Locate every Plasmodium falciparum-infected red blood cell.
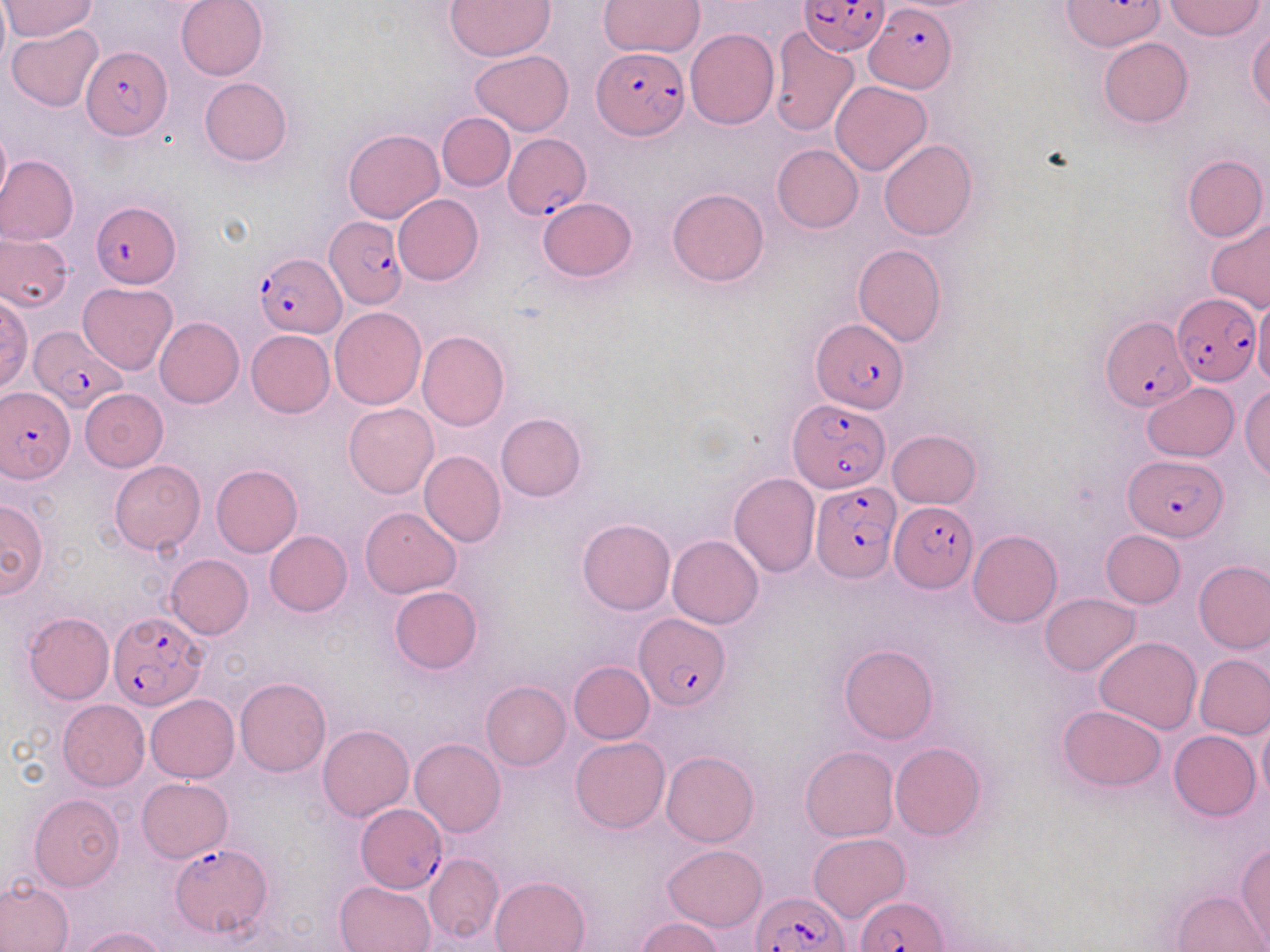
Approximate bounding boxes as named x1/y1/x2/y2 corners in pixels.
Plasmodium falciparum-infected red blood cells: (x1=800, y1=1, x2=890, y2=56), (x1=864, y1=6, x2=955, y2=92), (x1=79, y1=45, x2=172, y2=140), (x1=593, y1=46, x2=689, y2=139), (x1=504, y1=133, x2=593, y2=219), (x1=91, y1=200, x2=181, y2=287), (x1=325, y1=217, x2=407, y2=308), (x1=257, y1=254, x2=344, y2=337), (x1=1172, y1=294, x2=1260, y2=385), (x1=1099, y1=314, x2=1194, y2=412), (x1=809, y1=319, x2=909, y2=412), (x1=29, y1=323, x2=125, y2=412), (x1=2, y1=388, x2=74, y2=480), (x1=787, y1=397, x2=891, y2=492), (x1=1124, y1=454, x2=1228, y2=539), (x1=810, y1=480, x2=900, y2=582), (x1=888, y1=501, x2=974, y2=592), (x1=107, y1=610, x2=208, y2=711), (x1=634, y1=612, x2=731, y2=711), (x1=355, y1=804, x2=448, y2=892), (x1=169, y1=843, x2=274, y2=939), (x1=751, y1=891, x2=852, y2=952), (x1=853, y1=896, x2=947, y2=951).

Uninfected red blood cell locations: (x1=0, y1=0, x2=10, y2=69), (x1=175, y1=0, x2=269, y2=81), (x1=445, y1=0, x2=555, y2=59), (x1=1165, y1=0, x2=1264, y2=41), (x1=1, y1=1, x2=99, y2=42), (x1=598, y1=1, x2=705, y2=56), (x1=7, y1=24, x2=104, y2=112), (x1=769, y1=27, x2=860, y2=137), (x1=1247, y1=27, x2=1270, y2=113), (x1=685, y1=28, x2=780, y2=129), (x1=1098, y1=38, x2=1192, y2=128), (x1=469, y1=51, x2=573, y2=135), (x1=199, y1=77, x2=292, y2=166), (x1=832, y1=81, x2=932, y2=175), (x1=437, y1=112, x2=515, y2=192), (x1=0, y1=123, x2=12, y2=209), (x1=343, y1=128, x2=443, y2=222), (x1=878, y1=138, x2=978, y2=240), (x1=772, y1=144, x2=862, y2=233), (x1=0, y1=155, x2=78, y2=245), (x1=1181, y1=155, x2=1267, y2=242), (x1=667, y1=188, x2=768, y2=287), (x1=393, y1=194, x2=483, y2=285), (x1=536, y1=198, x2=636, y2=281), (x1=1206, y1=218, x2=1270, y2=313), (x1=1, y1=232, x2=72, y2=311), (x1=853, y1=244, x2=947, y2=346), (x1=79, y1=282, x2=177, y2=375), (x1=0, y1=293, x2=33, y2=393), (x1=1254, y1=296, x2=1270, y2=393), (x1=330, y1=307, x2=425, y2=409), (x1=154, y1=317, x2=244, y2=408), (x1=246, y1=330, x2=334, y2=417), (x1=417, y1=330, x2=510, y2=432), (x1=1141, y1=382, x2=1239, y2=462), (x1=1240, y1=386, x2=1269, y2=480), (x1=80, y1=389, x2=168, y2=470), (x1=344, y1=402, x2=438, y2=498), (x1=496, y1=412, x2=587, y2=501), (x1=887, y1=430, x2=981, y2=508), (x1=420, y1=450, x2=506, y2=548), (x1=109, y1=461, x2=204, y2=554), (x1=211, y1=464, x2=302, y2=557), (x1=729, y1=473, x2=819, y2=577), (x1=0, y1=499, x2=49, y2=597), (x1=359, y1=507, x2=462, y2=597), (x1=577, y1=518, x2=674, y2=615), (x1=1101, y1=530, x2=1186, y2=608), (x1=265, y1=531, x2=352, y2=616), (x1=968, y1=531, x2=1061, y2=627), (x1=668, y1=535, x2=763, y2=629), (x1=166, y1=555, x2=253, y2=639), (x1=1194, y1=561, x2=1270, y2=654), (x1=389, y1=586, x2=482, y2=674), (x1=1040, y1=593, x2=1139, y2=675), (x1=23, y1=612, x2=114, y2=704), (x1=1095, y1=636, x2=1202, y2=734), (x1=839, y1=645, x2=937, y2=744), (x1=1186, y1=654, x2=1265, y2=819), (x1=1194, y1=654, x2=1270, y2=738), (x1=569, y1=661, x2=654, y2=744), (x1=234, y1=678, x2=330, y2=776), (x1=481, y1=681, x2=571, y2=770), (x1=147, y1=694, x2=238, y2=782), (x1=57, y1=699, x2=149, y2=791), (x1=1057, y1=705, x2=1165, y2=791), (x1=1257, y1=714, x2=1270, y2=806), (x1=318, y1=725, x2=414, y2=821), (x1=1169, y1=729, x2=1260, y2=820), (x1=571, y1=737, x2=669, y2=833), (x1=409, y1=739, x2=505, y2=837), (x1=890, y1=742, x2=986, y2=840), (x1=800, y1=746, x2=898, y2=841), (x1=662, y1=750, x2=758, y2=846), (x1=137, y1=778, x2=233, y2=862), (x1=30, y1=793, x2=124, y2=891), (x1=808, y1=832, x2=910, y2=921), (x1=1236, y1=842, x2=1270, y2=948), (x1=663, y1=844, x2=766, y2=930), (x1=424, y1=853, x2=503, y2=944), (x1=489, y1=875, x2=589, y2=952), (x1=0, y1=879, x2=74, y2=951), (x1=334, y1=879, x2=436, y2=951), (x1=1173, y1=890, x2=1266, y2=951), (x1=635, y1=917, x2=725, y2=952), (x1=74, y1=925, x2=170, y2=952). Slide-level diagnosis: Plasmodium falciparum. May-Grünwald-Giemsa stain. Single field of view. Image is 1270×952 pixels. Captured at 1000x magnification. Thin blood smear. Light microscopy.